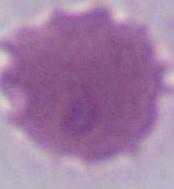

Summary:
  - Identification: erythrocyte
  - Magnification: 1000x
  - Modality: micrograph